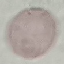

Result: no malaria parasites detected. Giemsa-stained preparation. Automatically extracted cell patch, resized to 64 × 64 pixels. Thin blood film. Acquired by smartphone through the microscope eyepiece.